Report the malaria status of this cell.
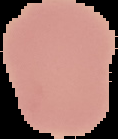
It is uninfected.

From a thin blood film. Segmented cell region on a black background. Image is 118×139 pixels.